Report the malaria status of this cell.
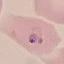
Parasitized.

Summary:
  - Stain: Giemsa
  - Capture: smartphone through the microscope eyepiece
  - Preparation: thin smear
  - Image type: automatically extracted cell patch, resized to 64 × 64 pixels